Name the parasite shown.
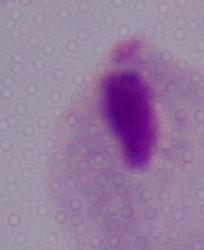

A trichomonad.

modality = micrograph
magnification = 1000x